Assess for malaria.
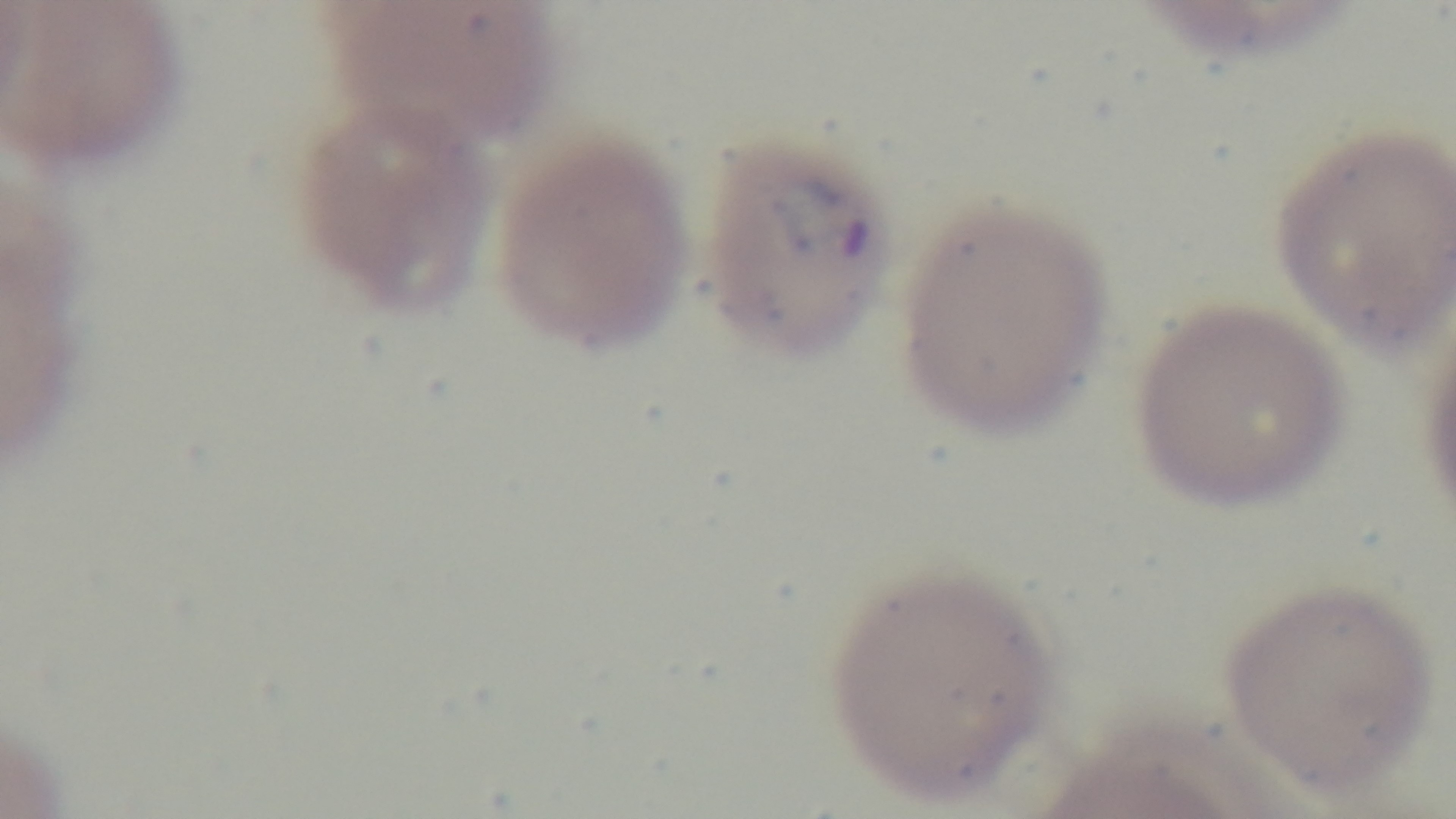

Infected.

field of view = single
capture = mounted 4K digital camera
stain = Giemsa
modality = light microscopy
preparation = thin
objective = 100x oil immersion